Assess this cell for malaria.
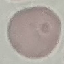
Uninfected.

capture = smartphone camera at the microscope eyepiece
image type = automatically extracted cell patch, resized to 64 × 64 pixels
stain = Giemsa
preparation = thin blood film